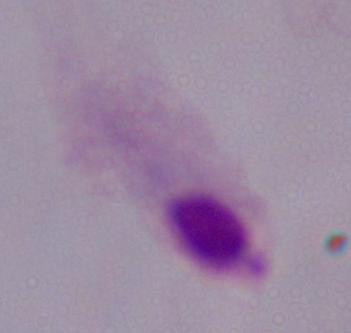
Photomicrograph. A trichomonad is seen. 1000x magnification.